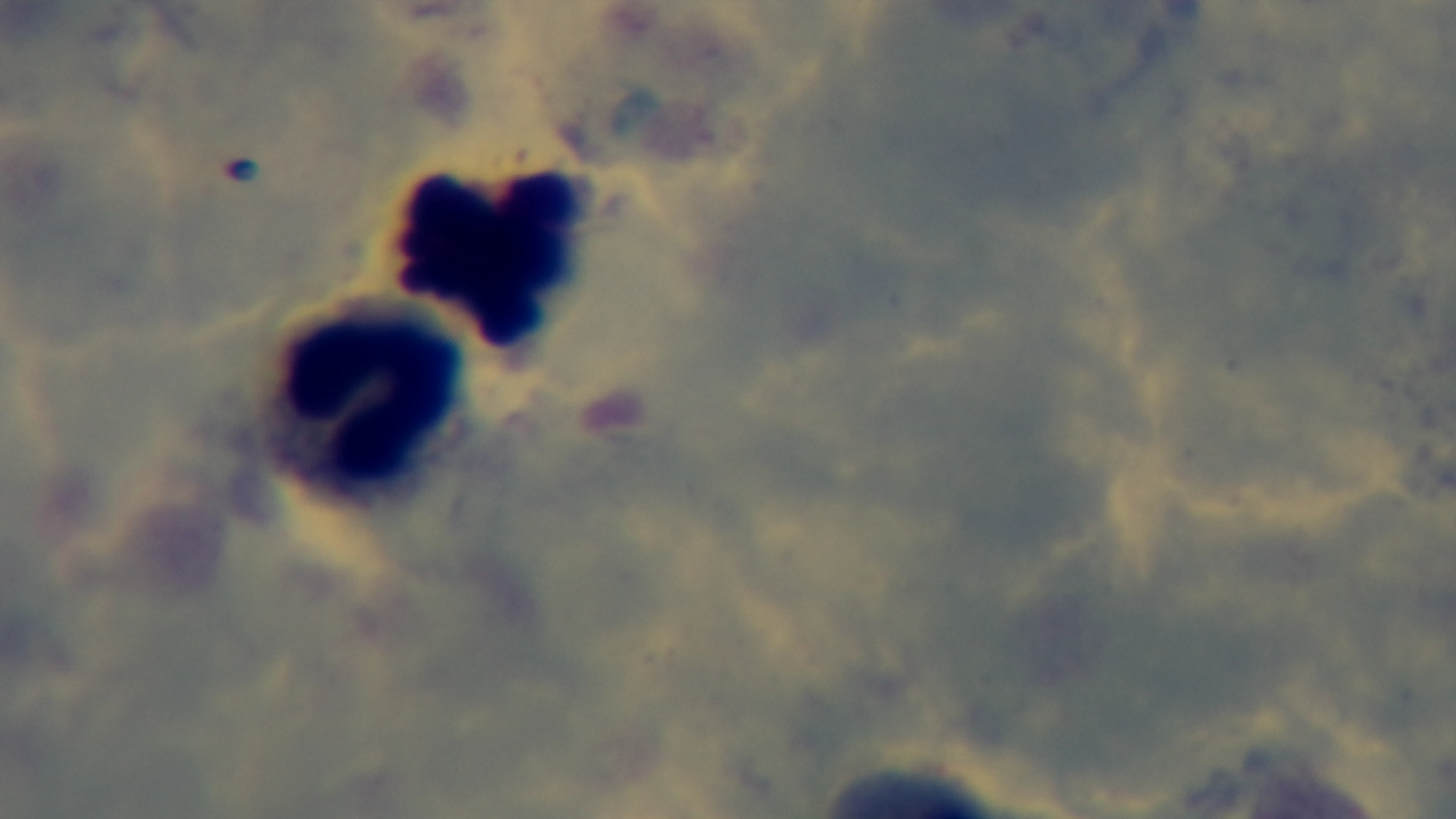

preparation = thick
field of view = one from the slide
malaria status = uninfected
modality = light microscopy
capture = mounted 4K digital camera
stain = Giemsa
objective = 100x oil immersion